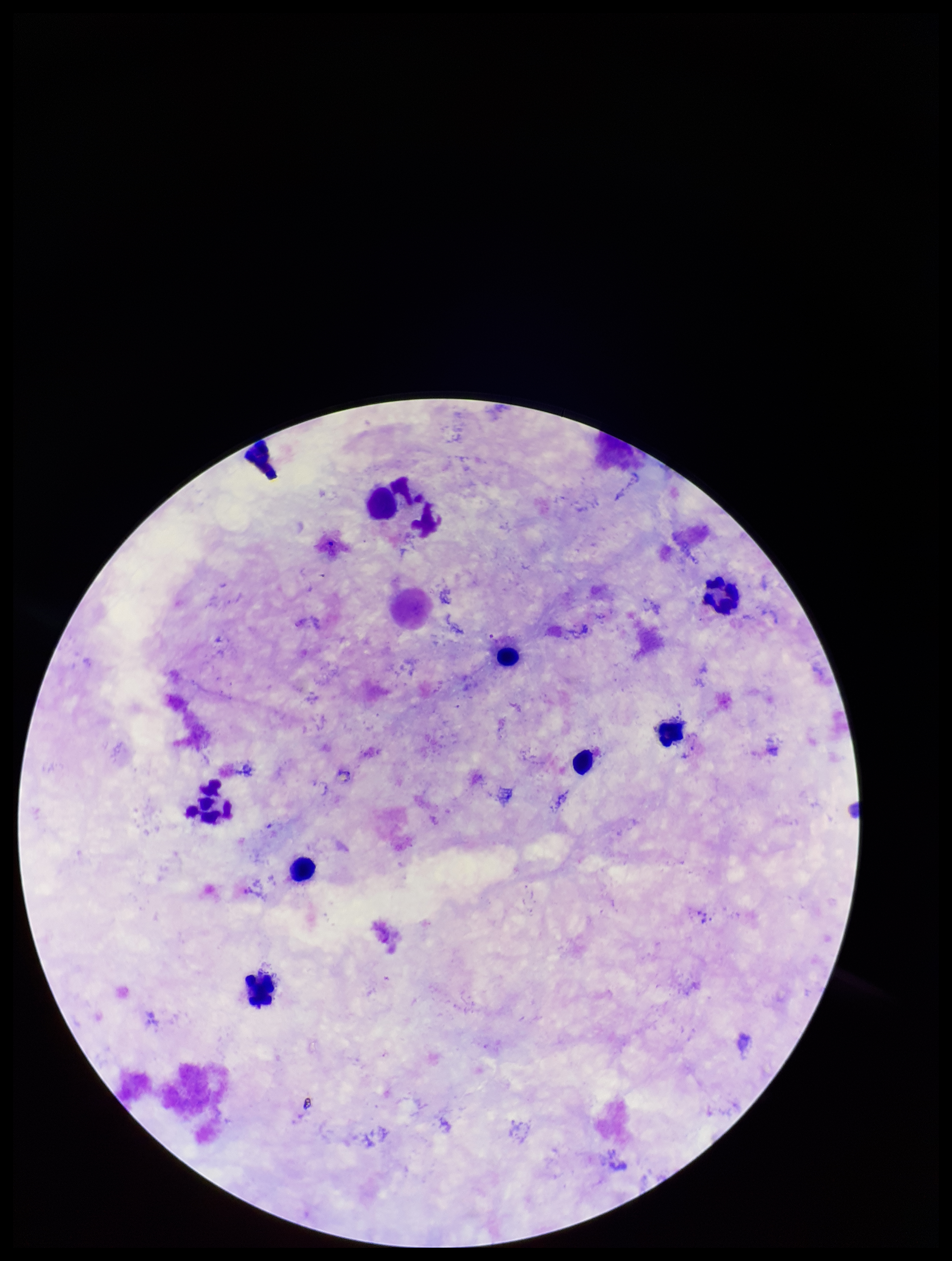
capture = smartphone photograph through the microscope eyepiece
field of view = one from this slide
parasite count = 0
preparation = thick
stain = Giemsa
image size = 952×1261 pixels
leukocyte count = 8
patient malaria status = negative
Plasmodium parasites = none identified